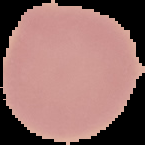
Summary:
  - Image size: 145×145 pixels
  - Malaria status: uninfected
  - Image type: segmented cell region on a black background
  - Preparation: thin blood smear